Classify this cell by malaria status.
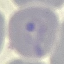

It is parasitized.

stain = Giemsa
image type = automatically extracted cell patch, resized to 64 × 64 pixels
capture = smartphone through the microscope eyepiece
preparation = thin blood film